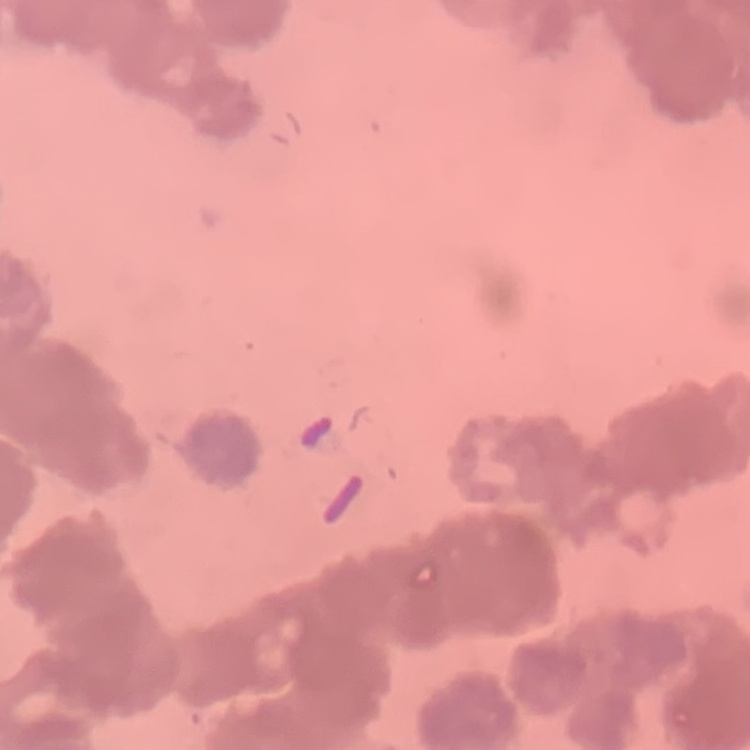
erythrocyte_morphology: rouleaux formation
stain: Field's or Giemsa
image_type: square crop of a larger photomicrograph
preparation: thin blood film